Describe the morphology of the red blood cells.
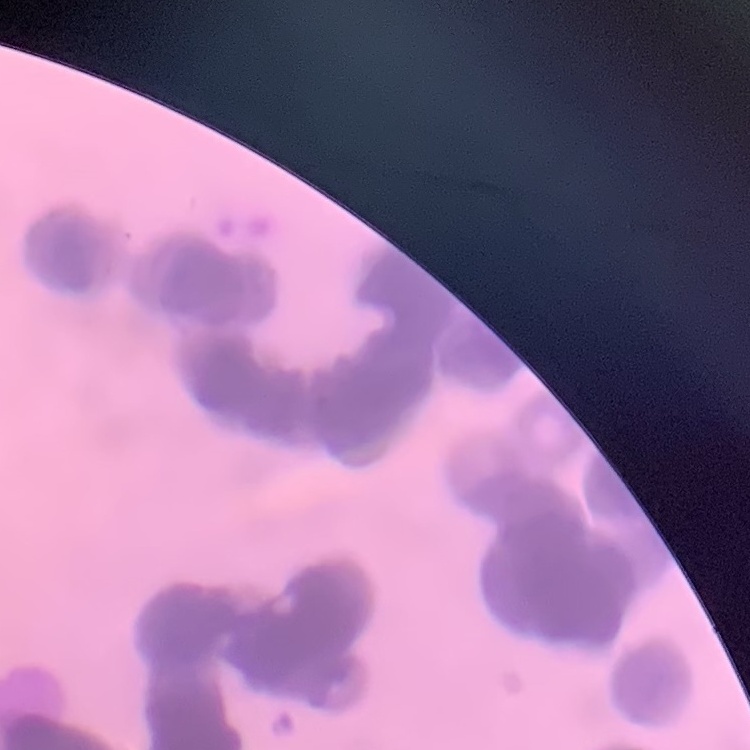
They show rouleaux formation.

One tile cut from a larger photomicrograph. Thin blood film. Stained with either Field's or Giemsa.